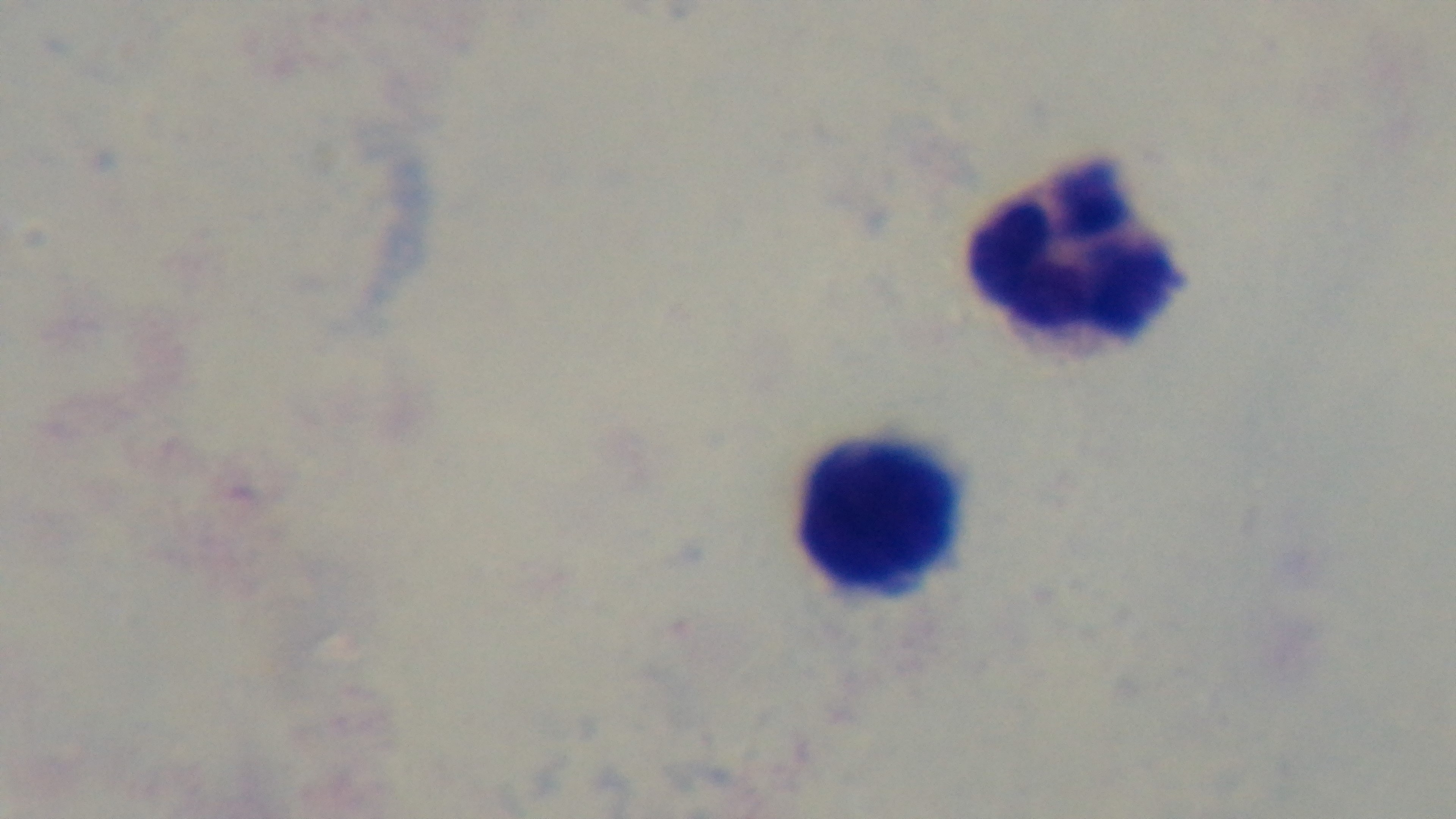
Oil-immersion objective, 100x. Malaria status: negative. Giemsa stain. Light microscopy. Captured with a mounted 4K digital camera. One field from the slide. Preparation: thick blood film.